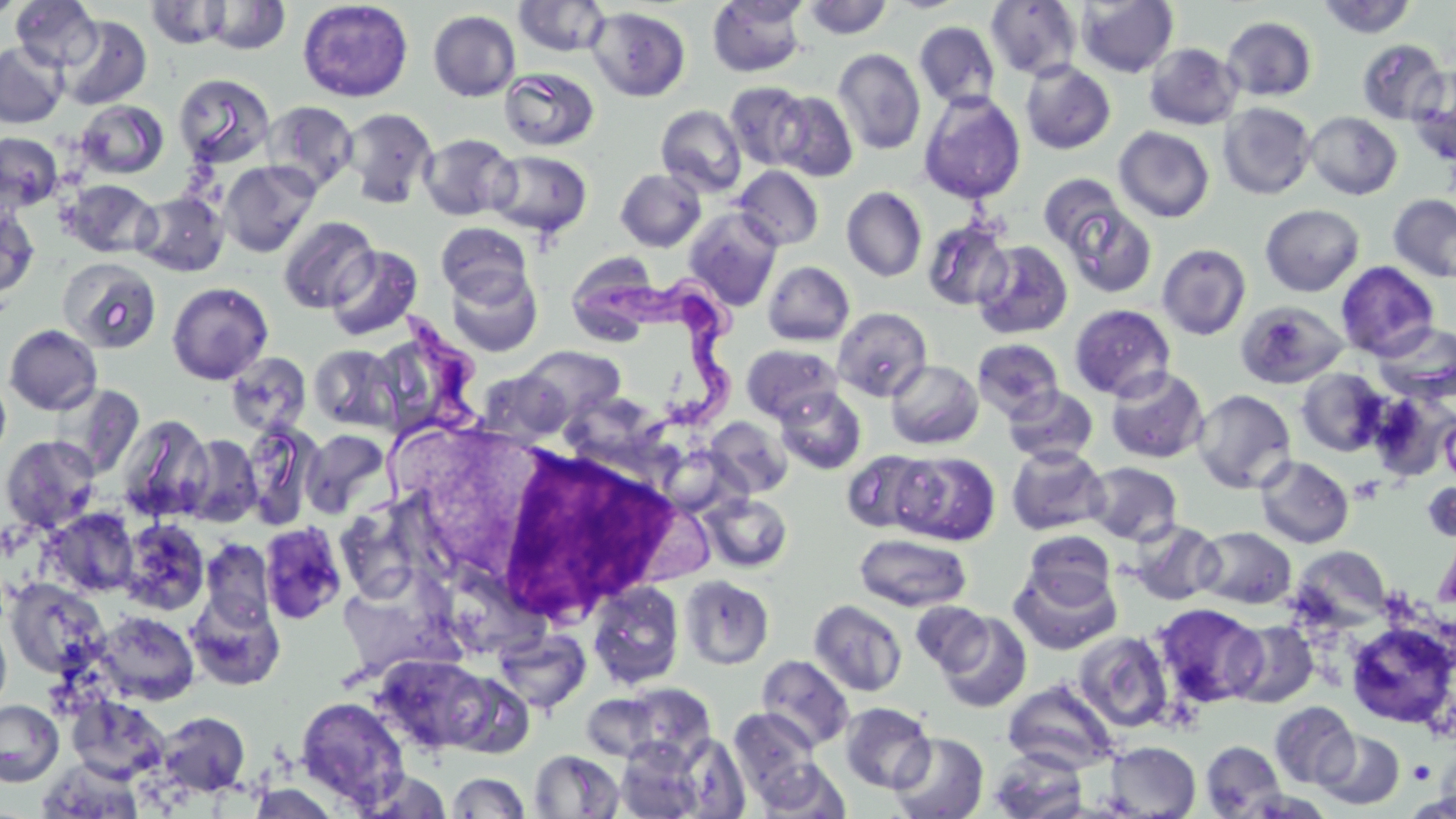

Trypanosoma brucei locations = approximate bounding boxes as (x1, y1, x2, y2) in pixels: (584, 262, 760, 444), (363, 312, 488, 523)
slide-level diagnosis = Trypanosoma brucei
platelet locations = approximate bounding boxes as (x1, y1, x2, y2) in pixels: (1349, 476, 1384, 504), (1407, 759, 1436, 784)
uninfected red blood cell locations = approximate bounding boxes as (x1, y1, x2, y2) in pixels: (0, 0, 26, 20), (297, 0, 414, 102), (802, 0, 893, 40), (985, 0, 1083, 81), (1076, 0, 1179, 77), (1316, 0, 1419, 39), (11, 1, 102, 71), (145, 1, 232, 49), (200, 1, 291, 55), (513, 1, 612, 58), (707, 1, 808, 77), (587, 6, 691, 101), (428, 10, 521, 102), (58, 15, 152, 110), (1221, 16, 1317, 102), (914, 21, 1001, 110), (1356, 40, 1449, 125), (1, 42, 68, 128), (1144, 43, 1242, 130), (833, 48, 926, 155), (1020, 61, 1115, 154), (1407, 65, 1456, 166), (499, 67, 599, 151), (173, 73, 276, 169), (724, 81, 812, 170), (771, 90, 859, 182), (918, 91, 1025, 205), (76, 99, 169, 179), (261, 100, 359, 194), (1218, 102, 1316, 200), (656, 105, 747, 197), (341, 107, 438, 208), (1304, 112, 1402, 200), (1114, 127, 1214, 223), (0, 132, 63, 212), (419, 132, 520, 221), (486, 149, 593, 239), (219, 160, 320, 257), (732, 165, 824, 250), (615, 168, 705, 251), (1039, 173, 1127, 254), (59, 179, 160, 259), (841, 186, 927, 282), (134, 191, 229, 277), (1388, 194, 1456, 283), (1062, 203, 1157, 298), (1067, 204, 1164, 402), (1260, 204, 1365, 296), (0, 206, 40, 300), (683, 207, 783, 310), (277, 216, 379, 313), (922, 218, 1014, 311), (435, 222, 532, 302), (972, 240, 1073, 340), (1158, 243, 1251, 340), (325, 245, 423, 341), (59, 258, 162, 353), (762, 261, 855, 346), (1336, 261, 1440, 359), (445, 265, 543, 357), (166, 281, 274, 385), (1235, 300, 1349, 389), (1069, 304, 1176, 401), (833, 307, 932, 401), (1373, 322, 1456, 405), (3, 324, 103, 415), (972, 338, 1064, 422), (308, 344, 401, 432), (742, 344, 842, 424), (519, 345, 626, 424), (224, 352, 312, 436), (885, 360, 983, 449), (1104, 366, 1209, 464), (1295, 368, 1390, 456), (0, 371, 11, 466), (52, 384, 145, 478), (1003, 385, 1099, 465), (774, 386, 867, 475), (1192, 389, 1296, 493), (1368, 390, 1456, 481), (117, 413, 213, 523), (1440, 414, 1456, 486), (704, 416, 792, 497), (242, 420, 322, 529), (301, 428, 391, 519), (1, 435, 100, 533), (182, 435, 262, 527), (1006, 444, 1109, 536), (842, 451, 935, 533), (893, 451, 1000, 545), (1255, 455, 1353, 548), (1084, 461, 1183, 545), (1424, 482, 1456, 543), (702, 493, 793, 573), (43, 508, 139, 598), (119, 518, 210, 616), (1127, 519, 1225, 606), (259, 521, 348, 625), (1195, 526, 1296, 609), (1023, 530, 1116, 607), (854, 532, 972, 612), (200, 538, 275, 628), (1289, 546, 1391, 629), (1008, 563, 1122, 655), (679, 575, 774, 670), (5, 578, 110, 678), (588, 581, 685, 689), (186, 591, 286, 691), (809, 600, 908, 697), (911, 600, 995, 676), (1153, 603, 1266, 708), (95, 611, 199, 704), (935, 611, 1032, 712), (0, 619, 11, 716), (1226, 619, 1319, 708), (1344, 620, 1455, 729), (493, 628, 591, 714), (1073, 631, 1174, 732), (373, 654, 495, 754), (757, 655, 855, 751), (1003, 680, 1120, 774), (620, 683, 716, 761), (582, 692, 663, 761), (67, 695, 170, 783), (296, 696, 409, 804), (0, 699, 64, 786), (1270, 701, 1358, 789), (840, 702, 936, 794), (730, 709, 819, 793), (156, 711, 250, 796), (1314, 729, 1405, 810), (889, 733, 987, 818), (676, 736, 750, 818), (616, 740, 708, 819), (1200, 740, 1287, 818), (1104, 741, 1200, 817), (529, 749, 624, 817), (987, 749, 1089, 819), (37, 758, 145, 819), (755, 759, 850, 817), (353, 769, 453, 818), (448, 772, 530, 818), (246, 784, 340, 818)
modality = light microscopy
magnification = 1000x
stain = May-Grünwald-Giemsa
image size = 1456×819 pixels
field of view = one of a larger specimen
preparation = thin blood film
white blood cell locations = approximate bounding boxes as (x1, y1, x2, y2) in pixels: (475, 440, 683, 624)